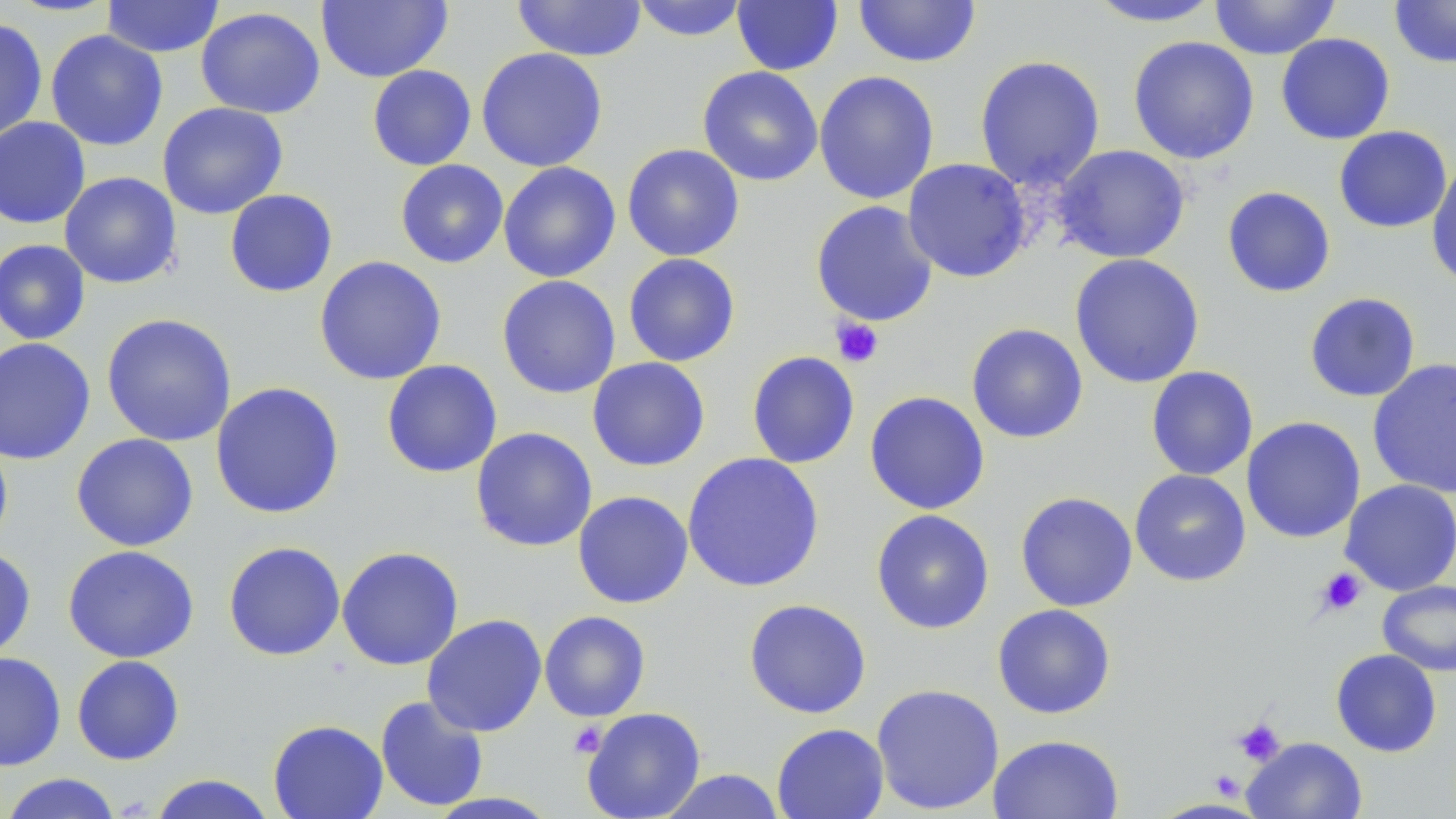

{
  "slide_level_diagnosis": "negative for blood parasites",
  "modality": "light microscopy",
  "image_size": "1456×819 pixels",
  "field_of_view": "one of a larger specimen",
  "stain": "May-Grünwald-Giemsa",
  "magnification": "1000x",
  "uninfected_red_blood_cell_locations": "approximate bounding boxes as [x1, y1, x2, y2] in pixels: [101, 0, 225, 58], [512, 0, 648, 62], [630, 0, 750, 42], [852, 0, 981, 68], [1084, 0, 1223, 28], [1209, 0, 1341, 60], [1389, 0, 1456, 69], [316, 1, 452, 83], [732, 1, 843, 76], [195, 6, 326, 119], [0, 18, 49, 144], [45, 30, 168, 151], [1276, 33, 1395, 145], [1128, 36, 1259, 165], [476, 47, 608, 172], [974, 55, 1106, 191], [367, 64, 477, 171], [697, 66, 824, 186], [813, 70, 940, 205], [157, 102, 288, 219], [0, 116, 91, 229], [1334, 126, 1452, 234], [621, 143, 745, 261], [1051, 144, 1191, 264], [499, 156, 744, 271], [902, 158, 1032, 283], [1427, 159, 1456, 291], [395, 160, 509, 268], [498, 161, 621, 283], [59, 171, 182, 289], [1222, 186, 1336, 298], [224, 189, 338, 297], [810, 200, 939, 327], [0, 239, 91, 345], [623, 253, 741, 367], [1069, 253, 1205, 389], [314, 255, 447, 385], [496, 275, 621, 399], [1304, 292, 1421, 402], [100, 313, 237, 447], [966, 323, 1089, 444], [0, 337, 96, 465], [746, 351, 860, 469], [587, 356, 711, 472], [1367, 358, 1456, 500], [381, 359, 503, 478], [1146, 366, 1258, 481], [210, 381, 345, 519], [864, 391, 990, 515], [1241, 416, 1366, 543], [470, 427, 598, 552], [0, 433, 13, 556], [71, 433, 199, 552], [682, 452, 825, 593], [1129, 469, 1251, 587], [1339, 479, 1456, 596], [572, 482, 822, 604], [572, 490, 694, 609], [1015, 491, 1138, 612], [871, 509, 995, 634], [223, 541, 346, 661], [62, 544, 199, 663], [336, 546, 464, 671], [0, 547, 36, 661], [1377, 580, 1456, 677], [743, 598, 872, 719], [992, 603, 1116, 719], [539, 610, 651, 722], [421, 614, 547, 737], [1331, 649, 1442, 757], [0, 651, 67, 772], [71, 655, 185, 765], [870, 683, 1005, 815], [375, 695, 490, 812], [581, 706, 706, 819], [268, 719, 389, 819], [771, 723, 889, 819], [987, 734, 1124, 819], [1242, 737, 1368, 819], [656, 768, 788, 819], [0, 772, 124, 819], [147, 773, 278, 819]",
  "preparation": "thin blood film",
  "platelet_locations": "approximate bounding boxes as [x1, y1, x2, y2] in pixels: [830, 318, 884, 368], [1315, 567, 1367, 616], [1233, 718, 1285, 765], [568, 721, 608, 758], [1210, 770, 1245, 800]"
}